Give the extent of all Plasmodium falciparum-infected red blood cells.
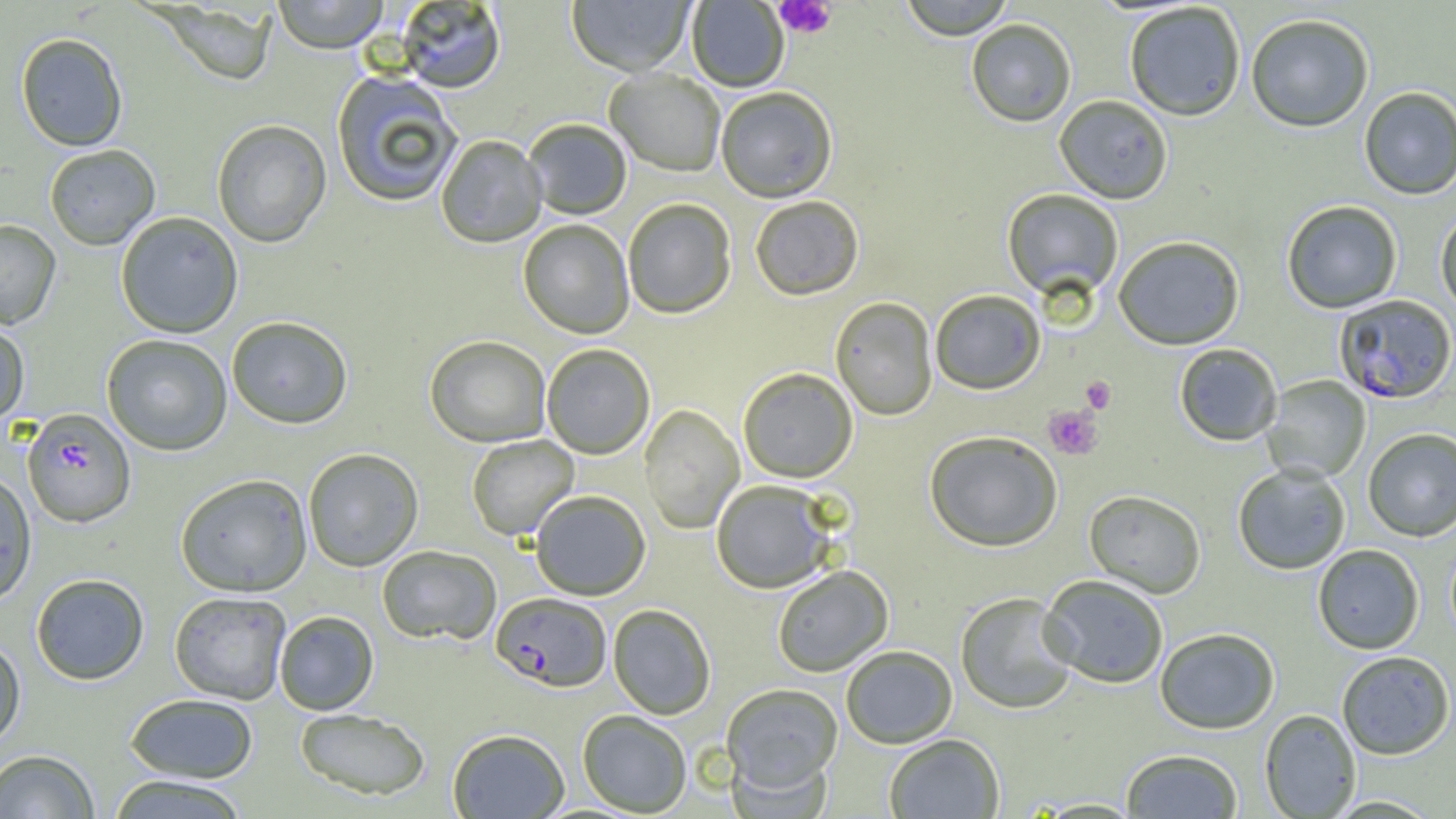
Approximate bounding boxes as (x1,y1)-(x2,y2) corner pairs in pixels.
Plasmodium falciparum-infected red blood cells: (1334,294)-(1456,405), (22,408)-(136,528), (491,593)-(611,693).

slide-level diagnosis = Plasmodium falciparum
magnification = 1000x
image size = 1456×819 pixels
preparation = thin blood smear
modality = light microscopy
field of view = one of a larger specimen
platelet locations = approximate bounding boxes as (x1,y1)-(x2,y2) corner pairs in pixels: (774,1)-(837,39), (1080,376)-(1116,413), (1043,406)-(1104,460)
uninfected red blood cell locations = approximate bounding boxes as (x1,y1)-(x2,y2) corner pairs in pixels: (272,0)-(389,55), (566,0)-(696,79), (898,0)-(1016,41), (687,1)-(789,93), (395,2)-(506,95), (156,3)-(277,87), (1124,3)-(1246,122), (1245,14)-(1374,134), (966,20)-(1077,129), (15,32)-(128,152), (604,70)-(725,178), (331,72)-(462,208), (1359,87)-(1456,200), (716,89)-(838,205), (1053,97)-(1173,206), (212,120)-(332,249), (523,120)-(631,221), (436,136)-(547,250), (44,145)-(160,251), (1001,190)-(1123,304), (751,197)-(864,302), (623,200)-(736,320), (1282,201)-(1402,314), (1435,209)-(1456,320), (115,212)-(243,339), (0,220)-(61,330), (518,220)-(634,340), (1113,238)-(1245,352), (930,291)-(1045,396), (830,297)-(938,422), (227,317)-(353,430), (0,320)-(30,428), (101,334)-(232,456), (425,336)-(551,448), (1174,344)-(1282,447), (541,345)-(655,460), (738,368)-(858,485), (1262,376)-(1371,483), (639,404)-(745,534), (1363,429)-(1456,542), (924,432)-(1062,553), (466,435)-(579,541), (303,449)-(424,572), (1232,464)-(1351,575), (0,470)-(37,606), (175,474)-(313,597), (711,481)-(835,595), (531,491)-(651,601), (1084,491)-(1206,599), (1313,544)-(1424,655), (377,546)-(501,647), (772,566)-(893,677), (31,573)-(149,685), (1039,576)-(1168,690), (169,591)-(291,705), (956,594)-(1077,715), (608,604)-(716,720), (274,611)-(379,715), (1155,630)-(1280,735), (0,634)-(26,750), (842,646)-(957,750), (1336,651)-(1454,761), (720,684)-(843,797), (125,693)-(258,783), (294,708)-(431,801), (578,710)-(691,816), (1259,710)-(1361,818), (448,729)-(569,819), (884,735)-(1005,818), (0,749)-(99,818), (1120,750)-(1243,818), (105,775)-(251,819), (1323,795)-(1444,817)